Name the parasite shown.
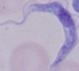
This is a trypanosome.

{
  "magnification": "1000x",
  "modality": "photomicrograph"
}